Evaluate for parasitized red blood cells.
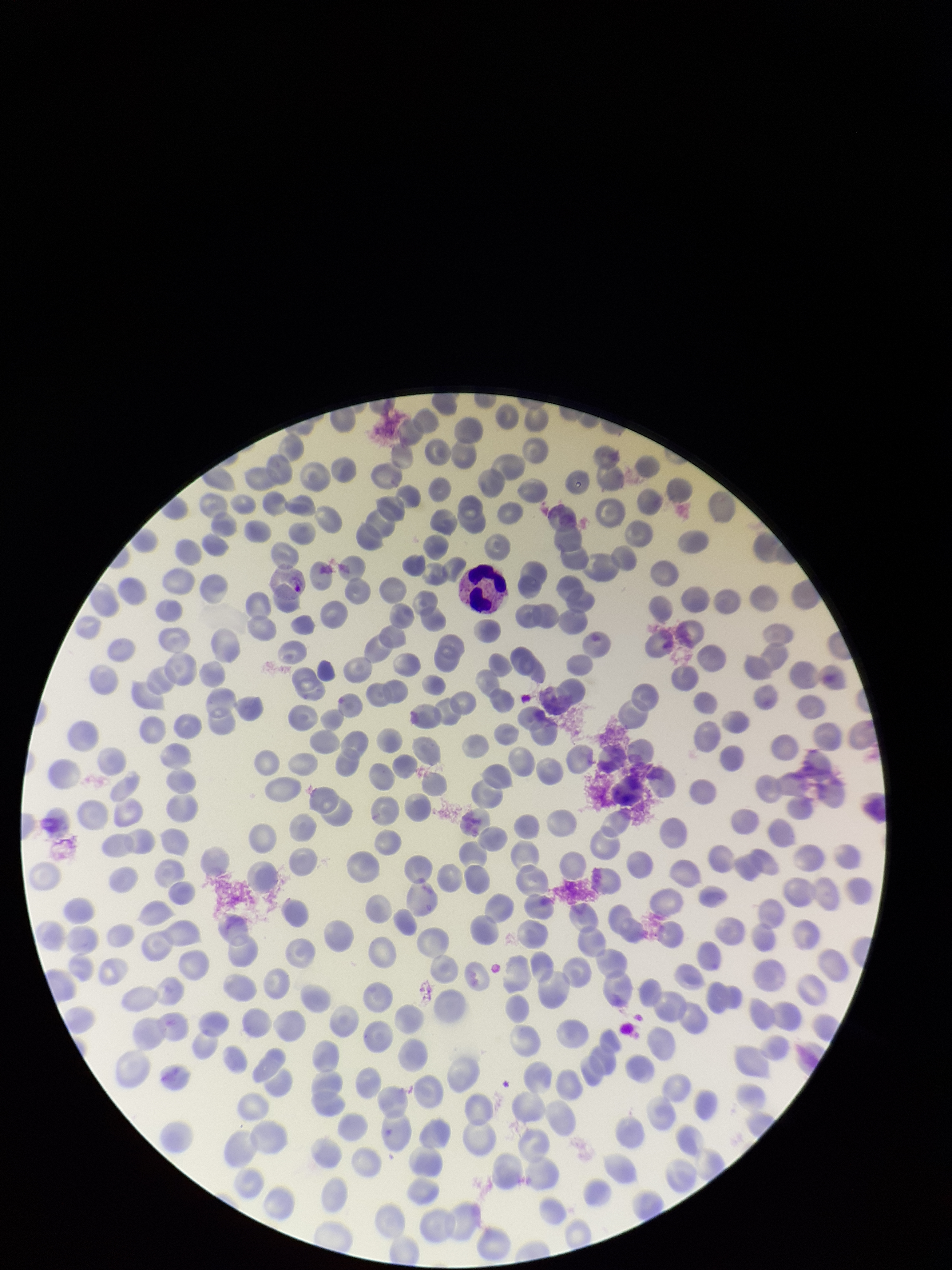

Identified.

preparation = thin smear
capture = smartphone photograph through the microscope eyepiece
parasitized red blood cell count = 1
field of view = single
patient malaria status = infected
red blood cell count = 298
image size = 952×1270 pixels
species reported for this patient = Plasmodium vivax
stain = Giemsa